Outline each blood parasite and name the species.
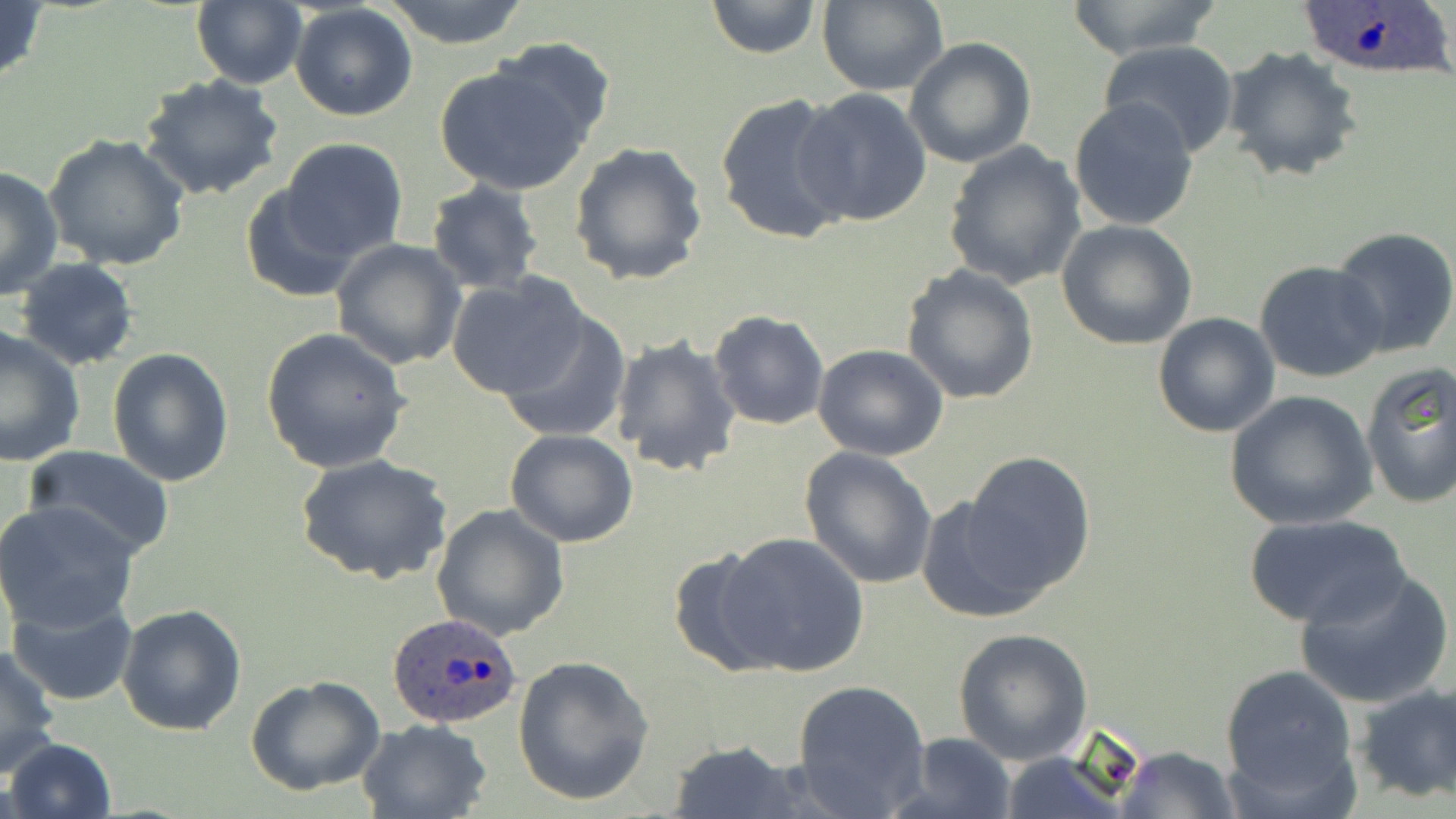
Approximate bounding boxes as named x1/y1/x2/y2 corners in pixels.
Plasmodium ovale-infected red blood cells: (x1=1295, y1=0, x2=1453, y2=79), (x1=386, y1=614, x2=524, y2=731).
No Plasmodium falciparum, Plasmodium malariae, Plasmodium vivax, Babesia divergens, or Trypanosoma brucei observed.

Uninfected red blood cell locations: (x1=0, y1=0, x2=49, y2=93), (x1=191, y1=0, x2=307, y2=89), (x1=379, y1=0, x2=530, y2=46), (x1=705, y1=0, x2=823, y2=58), (x1=1063, y1=0, x2=1222, y2=59), (x1=816, y1=1, x2=950, y2=97), (x1=289, y1=4, x2=418, y2=121), (x1=489, y1=35, x2=619, y2=150), (x1=905, y1=37, x2=1037, y2=170), (x1=1096, y1=40, x2=1241, y2=158), (x1=1218, y1=46, x2=1364, y2=183), (x1=433, y1=59, x2=597, y2=195), (x1=138, y1=74, x2=285, y2=205), (x1=794, y1=89, x2=933, y2=226), (x1=713, y1=90, x2=852, y2=246), (x1=1068, y1=98, x2=1199, y2=232), (x1=43, y1=133, x2=189, y2=271), (x1=279, y1=138, x2=409, y2=263), (x1=569, y1=140, x2=709, y2=287), (x1=942, y1=141, x2=1087, y2=290), (x1=0, y1=164, x2=62, y2=301), (x1=238, y1=179, x2=364, y2=304), (x1=426, y1=179, x2=545, y2=294), (x1=1055, y1=220, x2=1198, y2=350), (x1=1330, y1=227, x2=1456, y2=357), (x1=331, y1=239, x2=467, y2=371), (x1=14, y1=257, x2=139, y2=370), (x1=1254, y1=261, x2=1388, y2=384), (x1=899, y1=264, x2=1041, y2=405), (x1=447, y1=273, x2=587, y2=401), (x1=497, y1=309, x2=631, y2=444), (x1=708, y1=309, x2=830, y2=432), (x1=1152, y1=311, x2=1280, y2=437), (x1=0, y1=324, x2=86, y2=469), (x1=259, y1=327, x2=411, y2=473), (x1=610, y1=335, x2=742, y2=478), (x1=812, y1=345, x2=950, y2=461), (x1=106, y1=349, x2=235, y2=487), (x1=1358, y1=360, x2=1455, y2=508), (x1=1224, y1=390, x2=1377, y2=529), (x1=505, y1=428, x2=639, y2=547), (x1=24, y1=446, x2=175, y2=561), (x1=799, y1=446, x2=938, y2=590), (x1=960, y1=451, x2=1097, y2=593), (x1=296, y1=453, x2=453, y2=587), (x1=918, y1=496, x2=1046, y2=624), (x1=0, y1=501, x2=141, y2=632), (x1=430, y1=504, x2=569, y2=642), (x1=1244, y1=513, x2=1410, y2=630), (x1=716, y1=531, x2=870, y2=677), (x1=664, y1=547, x2=784, y2=676), (x1=1293, y1=567, x2=1453, y2=710), (x1=6, y1=594, x2=139, y2=707), (x1=117, y1=603, x2=247, y2=737), (x1=951, y1=627, x2=1095, y2=765), (x1=1, y1=642, x2=62, y2=775), (x1=512, y1=654, x2=655, y2=805), (x1=1219, y1=661, x2=1361, y2=811), (x1=245, y1=675, x2=386, y2=795), (x1=791, y1=679, x2=930, y2=816), (x1=1354, y1=681, x2=1455, y2=804), (x1=358, y1=718, x2=492, y2=819), (x1=895, y1=731, x2=1019, y2=819), (x1=5, y1=738, x2=116, y2=819), (x1=663, y1=742, x2=810, y2=818), (x1=1114, y1=745, x2=1240, y2=819), (x1=998, y1=754, x2=1138, y2=819). Slide-level diagnosis: Plasmodium ovale. Thin blood film. May-Grünwald-Giemsa-stained preparation. Image is 1456×819 pixels. Light microscopy. Captured at 1000x magnification. One field of a larger specimen.